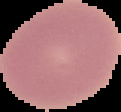
malaria_status: uninfected
image_type: cell region segmented out of the field of view; surrounding area masked to black
preparation: thin blood film
image_size: 121×112 pixels